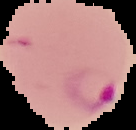
malaria status = parasitized
preparation = thin blood smear
image size = 136×130 pixels
image type = segmented cell region with the area outside set to black